Assess this cell for malaria.
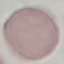
Uninfected.

Photographed with a smartphone camera at the microscope eyepiece. Giemsa-stained preparation. Thin blood smear. Automatically extracted cell patch, resized to 64 × 64 pixels.